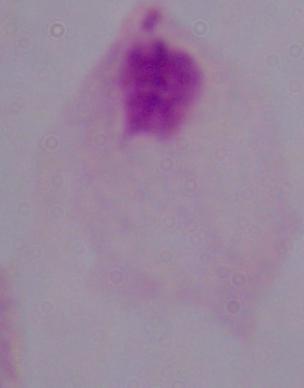

Micrograph. Captured at 1000x magnification. A trichomonad is seen.